Locate and identify every blood parasite.
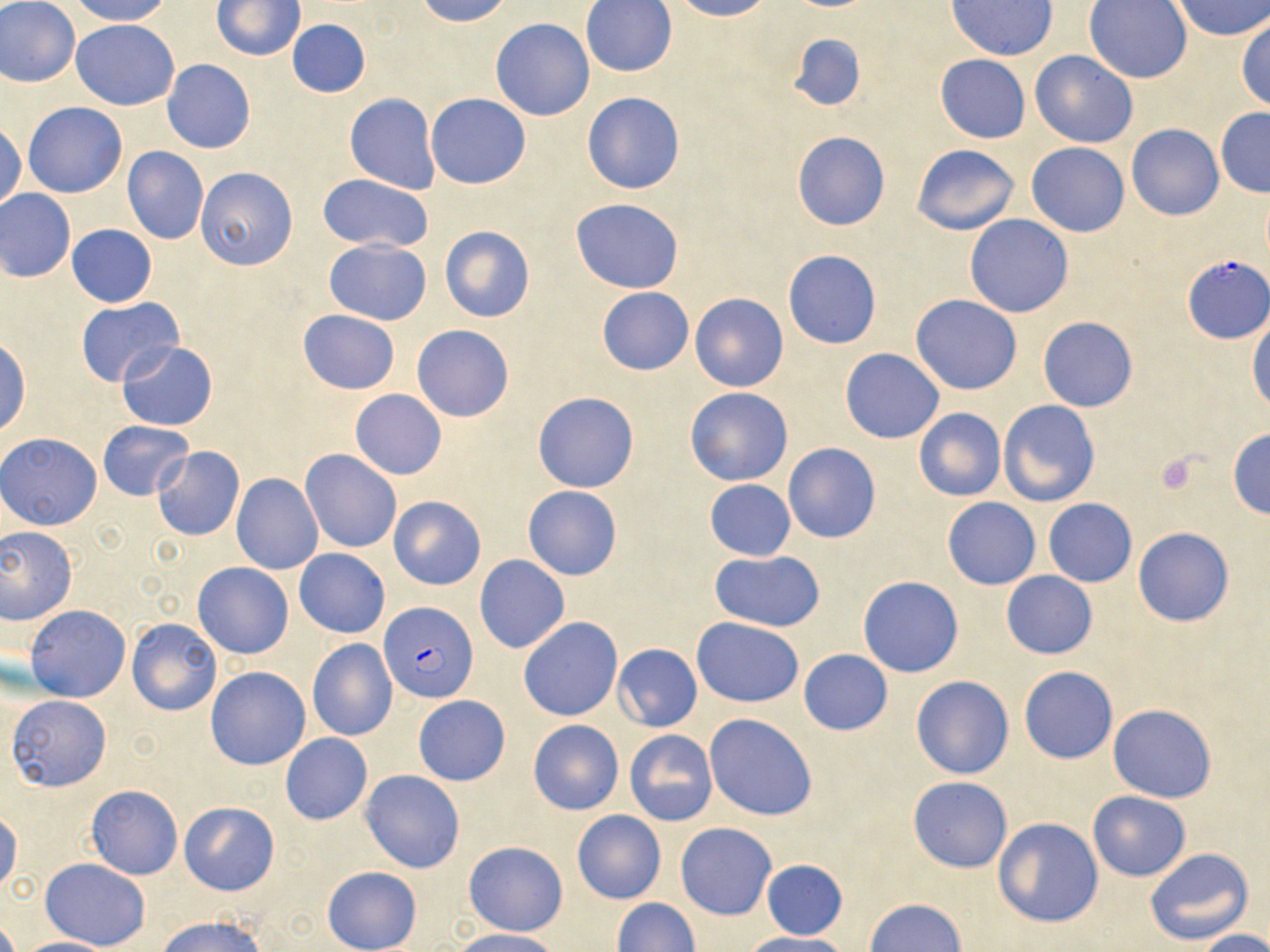
Approximate bounding boxes as (x1, y1, x2, y2) in pixels.
Plasmodium falciparum-infected red blood cells: (1182, 256, 1269, 342), (380, 602, 477, 703).
No Plasmodium ovale, Plasmodium malariae, Plasmodium vivax, Babesia divergens, or Trypanosoma brucei observed.

Summary:
  - Platelet locations: (1155, 452, 1206, 498)
  - Uninfected red blood cell locations: (0, 0, 81, 88), (68, 0, 174, 26), (414, 0, 513, 26), (580, 0, 678, 77), (670, 0, 775, 21), (1170, 0, 1269, 41), (213, 1, 304, 60), (949, 1, 1057, 60), (1084, 1, 1192, 84), (0, 6, 164, 94), (1235, 16, 1270, 114), (491, 18, 595, 120), (71, 19, 180, 110), (286, 19, 371, 97), (787, 33, 868, 111), (1029, 50, 1138, 148), (935, 54, 1031, 144), (163, 60, 255, 154), (581, 92, 684, 196), (344, 93, 441, 194), (425, 93, 531, 190), (23, 102, 127, 198), (1215, 108, 1270, 197), (0, 122, 24, 211), (1125, 123, 1224, 220), (792, 131, 891, 231), (1026, 142, 1130, 236), (911, 144, 1019, 234), (122, 146, 208, 244), (197, 167, 298, 270), (314, 174, 434, 253), (0, 188, 76, 282), (569, 198, 684, 293), (964, 214, 1073, 318), (66, 224, 157, 307), (441, 227, 534, 323), (323, 239, 431, 325), (782, 250, 881, 349), (596, 287, 695, 375), (691, 292, 788, 391), (910, 295, 1022, 395), (76, 298, 183, 388), (297, 309, 399, 394), (1247, 314, 1270, 413), (1037, 317, 1137, 412), (411, 325, 515, 423), (117, 339, 218, 431), (0, 340, 30, 437), (840, 349, 944, 444), (685, 387, 793, 486), (349, 389, 447, 479), (533, 392, 639, 493), (998, 399, 1099, 508), (913, 407, 1007, 502), (97, 421, 193, 500), (1227, 429, 1270, 518), (1, 432, 103, 530), (782, 443, 880, 544), (151, 447, 245, 540), (301, 448, 401, 553), (231, 473, 323, 576), (704, 479, 795, 560), (523, 485, 622, 581), (389, 496, 485, 589), (943, 497, 1040, 589), (1044, 498, 1136, 587), (0, 526, 77, 624), (1134, 527, 1233, 627), (294, 549, 390, 638), (708, 550, 826, 632), (476, 555, 569, 653), (194, 563, 293, 658), (1001, 571, 1097, 659), (857, 576, 964, 678), (25, 605, 131, 702), (518, 617, 623, 721), (127, 618, 221, 715), (692, 618, 804, 706), (307, 638, 398, 741), (612, 643, 702, 731), (798, 650, 892, 736), (1019, 666, 1117, 764), (206, 667, 310, 770), (911, 675, 1014, 780), (7, 694, 113, 791), (413, 695, 510, 786), (1109, 705, 1216, 802), (704, 713, 818, 821), (527, 718, 625, 815), (625, 730, 717, 826), (280, 734, 373, 824), (360, 770, 465, 873), (908, 776, 1013, 873), (86, 784, 184, 880), (1088, 790, 1190, 881), (180, 801, 280, 896), (0, 806, 21, 895), (571, 810, 666, 904), (993, 817, 1103, 928), (675, 822, 777, 920), (464, 841, 569, 937), (1144, 847, 1253, 947), (40, 858, 150, 949), (761, 860, 848, 940), (322, 865, 420, 952), (866, 898, 966, 951), (613, 899, 700, 952), (156, 915, 269, 952), (450, 929, 560, 952), (1197, 929, 1270, 952), (740, 932, 848, 952), (14, 937, 118, 952)
  - Slide-level diagnosis: Plasmodium falciparum
  - Preparation: thin blood smear
  - Stain: May-Grünwald-Giemsa
  - Modality: light microscopy
  - Image size: 1270×952 pixels
  - Magnification: 1000x
  - Field of view: one of a larger specimen